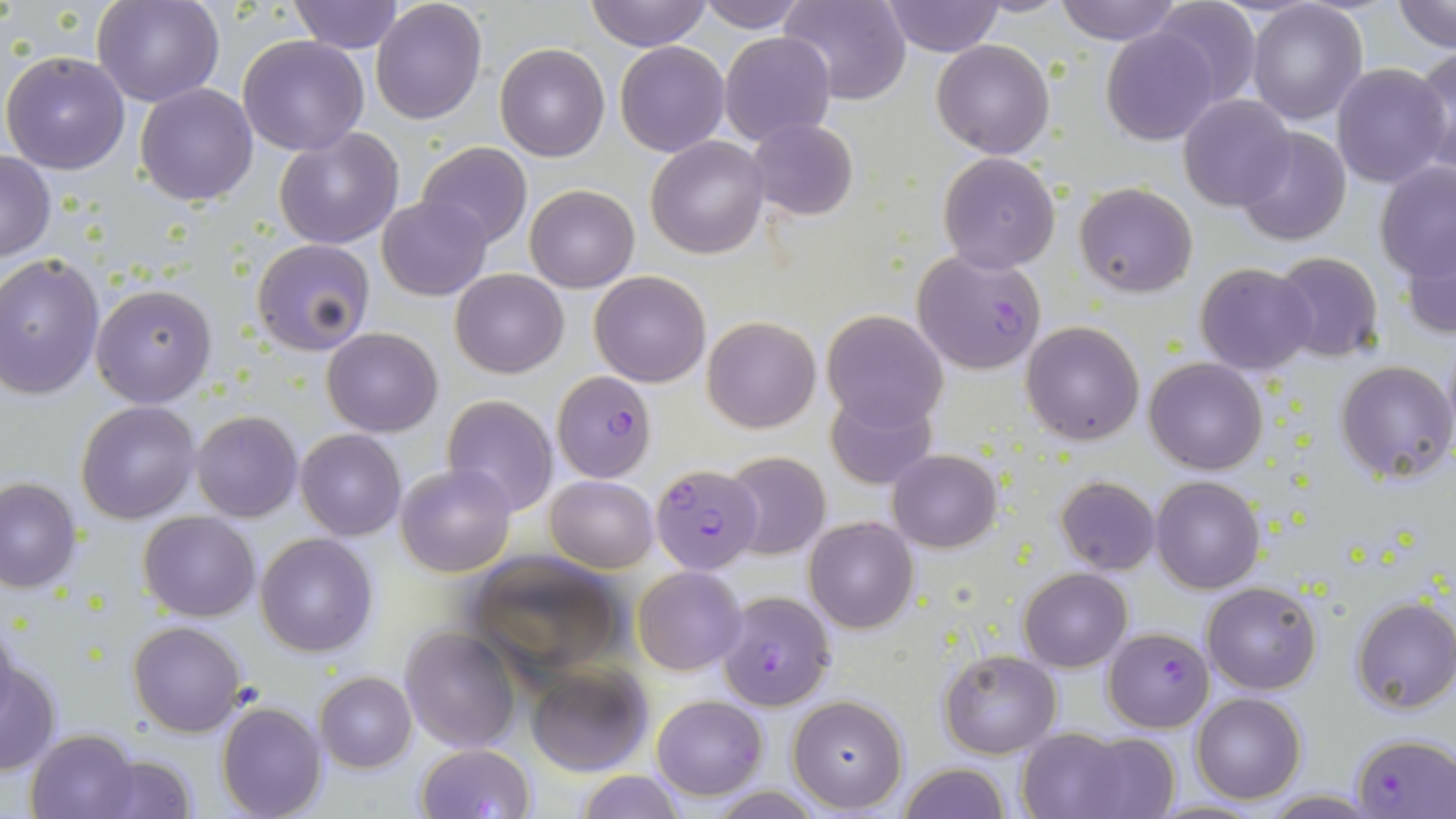
Summary:
  - Coordinate format: approximate bounding boxes as named x1/y1/x2/y2 corners in pixels
  - Plasmodium falciparum-infected red blood cell locations: (x1=912, y1=249, x2=1047, y2=376), (x1=553, y1=370, x2=657, y2=482), (x1=650, y1=462, x2=764, y2=574), (x1=717, y1=592, x2=835, y2=710), (x1=1105, y1=627, x2=1215, y2=731), (x1=1351, y1=733, x2=1455, y2=817)
  - Uninfected red blood cell locations: (x1=93, y1=0, x2=222, y2=107), (x1=285, y1=0, x2=405, y2=53), (x1=371, y1=0, x2=487, y2=122), (x1=586, y1=0, x2=709, y2=50), (x1=781, y1=0, x2=911, y2=104), (x1=1052, y1=0, x2=1183, y2=45), (x1=1150, y1=0, x2=1261, y2=109), (x1=1246, y1=0, x2=1368, y2=124), (x1=1393, y1=0, x2=1455, y2=51), (x1=695, y1=1, x2=810, y2=31), (x1=882, y1=1, x2=1004, y2=55), (x1=1103, y1=26, x2=1216, y2=147), (x1=718, y1=30, x2=836, y2=146), (x1=238, y1=35, x2=369, y2=155), (x1=931, y1=39, x2=1054, y2=158), (x1=615, y1=40, x2=729, y2=157), (x1=494, y1=44, x2=609, y2=162), (x1=1412, y1=44, x2=1456, y2=179), (x1=1, y1=50, x2=131, y2=175), (x1=1331, y1=62, x2=1454, y2=189), (x1=135, y1=83, x2=258, y2=206), (x1=1176, y1=94, x2=1292, y2=211), (x1=746, y1=117, x2=858, y2=221), (x1=1234, y1=126, x2=1353, y2=246), (x1=274, y1=127, x2=404, y2=250), (x1=646, y1=136, x2=768, y2=258), (x1=416, y1=142, x2=531, y2=250), (x1=1, y1=151, x2=56, y2=262), (x1=937, y1=151, x2=1061, y2=273), (x1=1375, y1=163, x2=1455, y2=281), (x1=1074, y1=182, x2=1198, y2=299), (x1=525, y1=184, x2=639, y2=293), (x1=377, y1=197, x2=491, y2=300), (x1=1402, y1=228, x2=1456, y2=342), (x1=251, y1=240, x2=375, y2=355), (x1=1270, y1=252, x2=1385, y2=362), (x1=0, y1=254, x2=104, y2=401), (x1=1195, y1=262, x2=1317, y2=375), (x1=450, y1=267, x2=569, y2=378), (x1=590, y1=270, x2=710, y2=387), (x1=90, y1=282, x2=217, y2=408), (x1=821, y1=310, x2=948, y2=431), (x1=702, y1=315, x2=821, y2=433), (x1=1022, y1=319, x2=1146, y2=446), (x1=322, y1=327, x2=442, y2=436), (x1=1144, y1=357, x2=1268, y2=475), (x1=1334, y1=359, x2=1455, y2=485), (x1=825, y1=388, x2=937, y2=490), (x1=442, y1=395, x2=558, y2=516), (x1=76, y1=400, x2=201, y2=522), (x1=191, y1=410, x2=303, y2=522), (x1=295, y1=429, x2=406, y2=540), (x1=887, y1=449, x2=1002, y2=552), (x1=721, y1=450, x2=830, y2=560), (x1=395, y1=462, x2=516, y2=576), (x1=0, y1=475, x2=83, y2=592), (x1=546, y1=475, x2=657, y2=571), (x1=1055, y1=476, x2=1160, y2=576), (x1=1151, y1=476, x2=1264, y2=592), (x1=138, y1=511, x2=260, y2=622), (x1=804, y1=516, x2=918, y2=634), (x1=256, y1=533, x2=378, y2=658), (x1=467, y1=551, x2=625, y2=676), (x1=632, y1=566, x2=747, y2=676), (x1=1019, y1=568, x2=1132, y2=672), (x1=1203, y1=581, x2=1321, y2=695), (x1=1350, y1=597, x2=1456, y2=716), (x1=128, y1=620, x2=246, y2=737), (x1=401, y1=625, x2=521, y2=753), (x1=939, y1=649, x2=1062, y2=758), (x1=1, y1=656, x2=62, y2=777), (x1=524, y1=660, x2=655, y2=775), (x1=314, y1=672, x2=416, y2=773), (x1=1190, y1=692, x2=1305, y2=804), (x1=652, y1=694, x2=767, y2=800), (x1=787, y1=694, x2=909, y2=813), (x1=216, y1=701, x2=328, y2=819), (x1=1015, y1=727, x2=1140, y2=818), (x1=27, y1=728, x2=142, y2=819), (x1=1062, y1=731, x2=1182, y2=818), (x1=415, y1=742, x2=536, y2=818), (x1=85, y1=752, x2=198, y2=819), (x1=897, y1=762, x2=1012, y2=819), (x1=577, y1=770, x2=685, y2=819), (x1=1260, y1=791, x2=1382, y2=817), (x1=1152, y1=799, x2=1267, y2=818)
  - Slide-level diagnosis: Plasmodium falciparum
  - Field of view: single
  - Modality: optical microscopy
  - Stain: May-Grünwald-Giemsa
  - Image size: 1456×819 pixels
  - Magnification: 1000x
  - Preparation: thin blood film